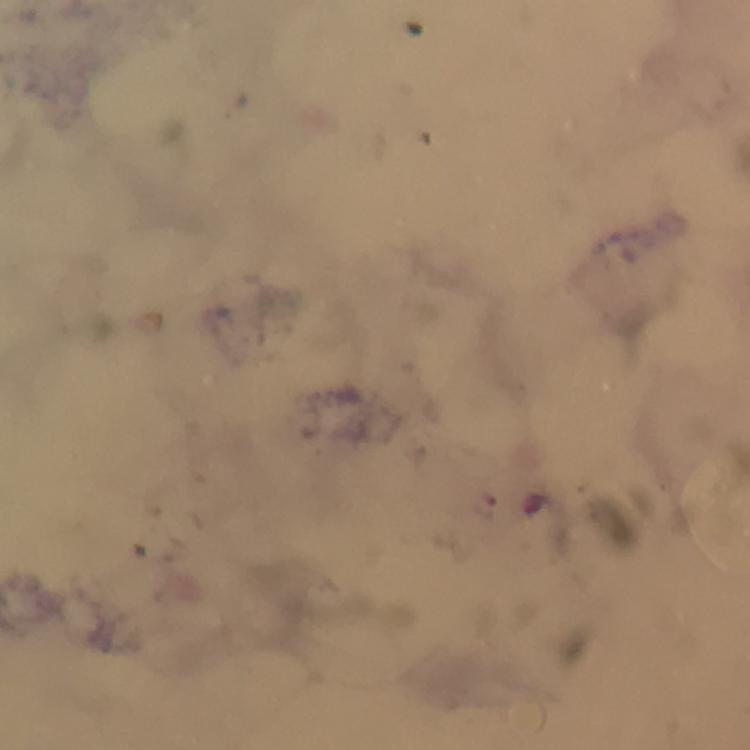
{
  "context": "from a diagnostic examination for malaria",
  "capture": "smartphone photograph through a microscope",
  "cropped_from": "one field of view",
  "stain": "Giemsa",
  "immersion_oil": "applied",
  "magnification": "100x",
  "preparation": "thick blood smear",
  "plasmodium_parasite_locations": "approximate object centers, in pixels from the top-left corner: (x=487, y=506)",
  "image_size": "750×750 pixels"
}